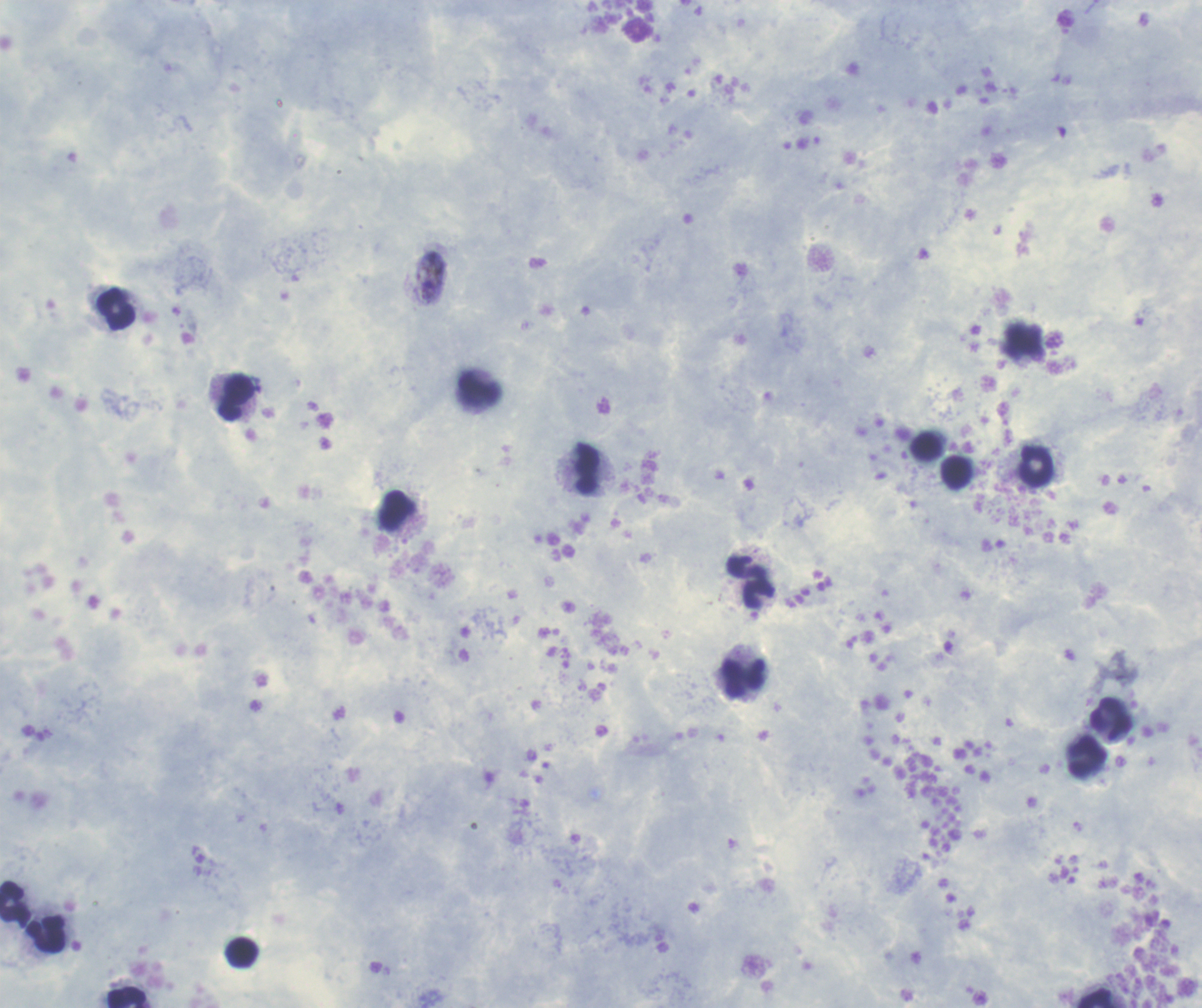 Coloration quality: good. Image is 1202×1008 pixels. Thick blood smear. Romanowsky stain. One field from this slide.